Assess for malaria.
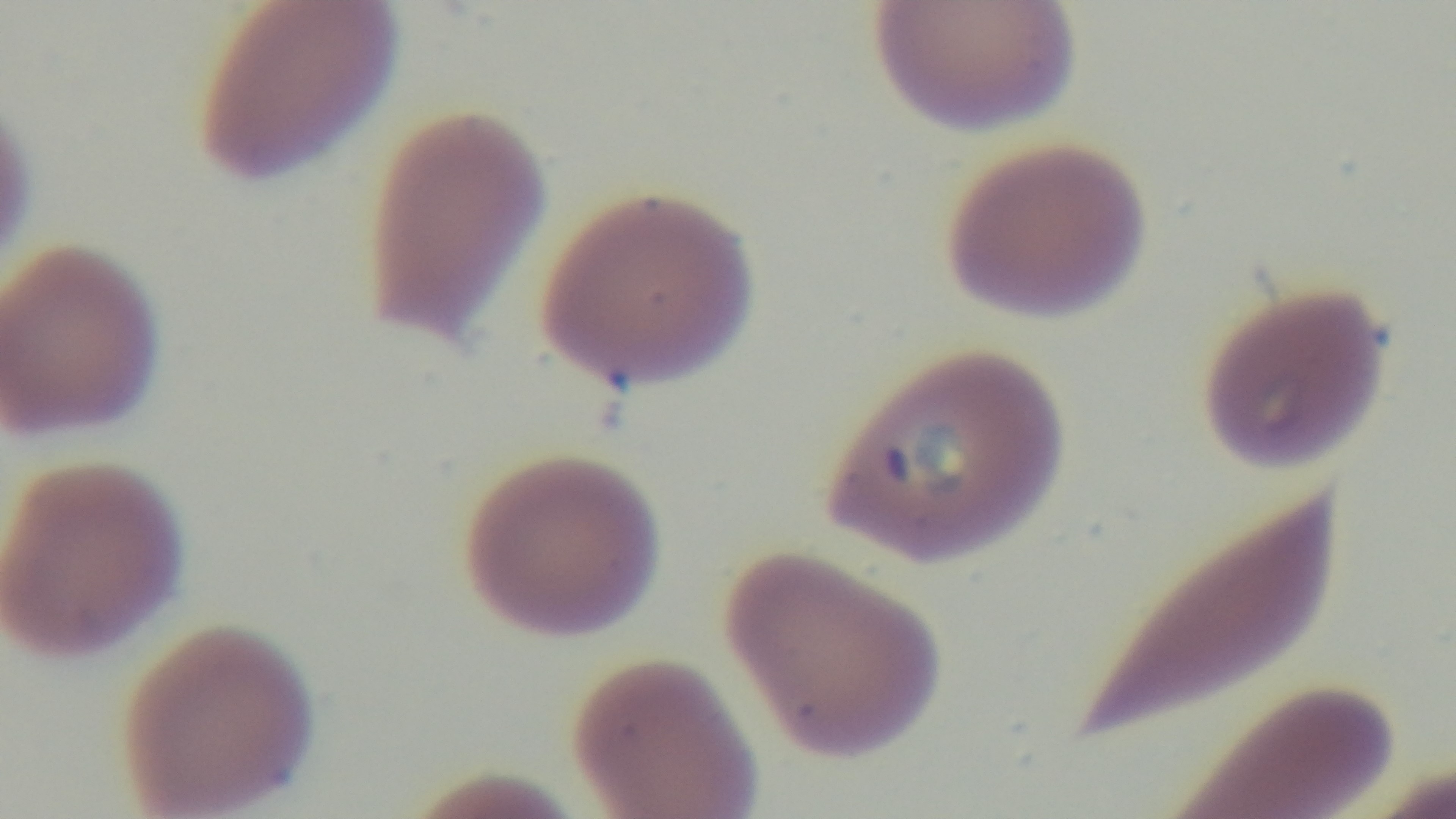

It is infected.

{
  "objective": "100x oil immersion",
  "preparation": "thin smear",
  "modality": "light microscopy",
  "field_of_view": "single",
  "capture": "mounted 4K digital camera",
  "stain": "Giemsa"
}